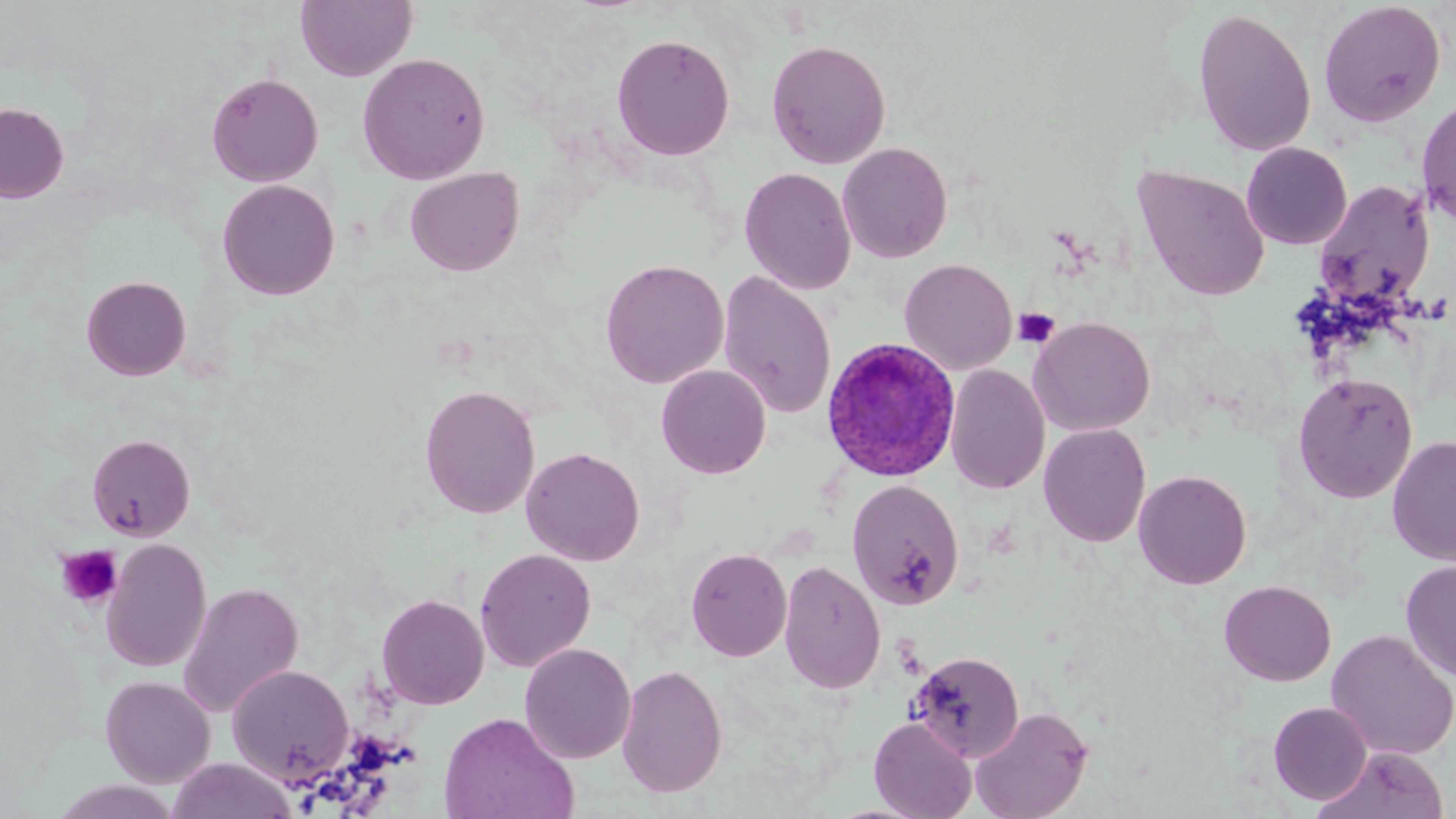

Summary:
  - Coordinate format: approximate bounding boxes as named x1/y1/x2/y2 corners in pixels
  - Uninfected red blood cell locations: (x1=295, y1=0, x2=417, y2=82), (x1=1318, y1=1, x2=1446, y2=128), (x1=1192, y1=8, x2=1317, y2=158), (x1=611, y1=33, x2=736, y2=161), (x1=766, y1=39, x2=891, y2=169), (x1=356, y1=51, x2=491, y2=185), (x1=205, y1=72, x2=324, y2=187), (x1=1415, y1=97, x2=1456, y2=229), (x1=0, y1=101, x2=69, y2=203), (x1=837, y1=142, x2=953, y2=263), (x1=1241, y1=142, x2=1353, y2=250), (x1=1132, y1=164, x2=1270, y2=301), (x1=404, y1=166, x2=525, y2=277), (x1=739, y1=167, x2=856, y2=295), (x1=217, y1=179, x2=340, y2=301), (x1=1312, y1=179, x2=1436, y2=312), (x1=899, y1=258, x2=1017, y2=375), (x1=599, y1=259, x2=729, y2=388), (x1=717, y1=271, x2=837, y2=420), (x1=81, y1=275, x2=192, y2=381), (x1=1028, y1=316, x2=1155, y2=436), (x1=656, y1=364, x2=772, y2=479), (x1=945, y1=364, x2=1050, y2=495), (x1=1292, y1=371, x2=1418, y2=504), (x1=419, y1=384, x2=540, y2=519), (x1=1038, y1=423, x2=1151, y2=547), (x1=86, y1=433, x2=196, y2=541), (x1=1387, y1=435, x2=1456, y2=565), (x1=521, y1=446, x2=645, y2=566), (x1=1133, y1=469, x2=1252, y2=589), (x1=846, y1=479, x2=965, y2=610), (x1=100, y1=538, x2=212, y2=673), (x1=685, y1=547, x2=792, y2=662), (x1=475, y1=548, x2=596, y2=673), (x1=1399, y1=558, x2=1456, y2=683), (x1=778, y1=559, x2=886, y2=694), (x1=1219, y1=580, x2=1337, y2=687), (x1=177, y1=582, x2=304, y2=718), (x1=376, y1=593, x2=489, y2=709), (x1=1326, y1=629, x2=1456, y2=761), (x1=519, y1=643, x2=636, y2=763), (x1=909, y1=650, x2=1025, y2=763), (x1=617, y1=663, x2=728, y2=798), (x1=227, y1=664, x2=354, y2=784), (x1=100, y1=675, x2=216, y2=787), (x1=1269, y1=701, x2=1373, y2=804), (x1=969, y1=705, x2=1093, y2=819), (x1=438, y1=711, x2=580, y2=819), (x1=869, y1=715, x2=977, y2=819), (x1=1313, y1=745, x2=1450, y2=819), (x1=167, y1=758, x2=297, y2=819), (x1=47, y1=779, x2=182, y2=819)
  - Platelet locations: (x1=1013, y1=307, x2=1060, y2=349), (x1=55, y1=544, x2=124, y2=610)
  - Plasmodium ovale-infected red blood cell locations: (x1=821, y1=338, x2=960, y2=482)
  - Slide-level diagnosis: Plasmodium ovale
  - Modality: optical microscopy
  - Image size: 1456×819 pixels
  - Preparation: thin blood smear
  - Magnification: 1000x
  - Stain: May-Grünwald-Giemsa
  - Field of view: one of a larger specimen